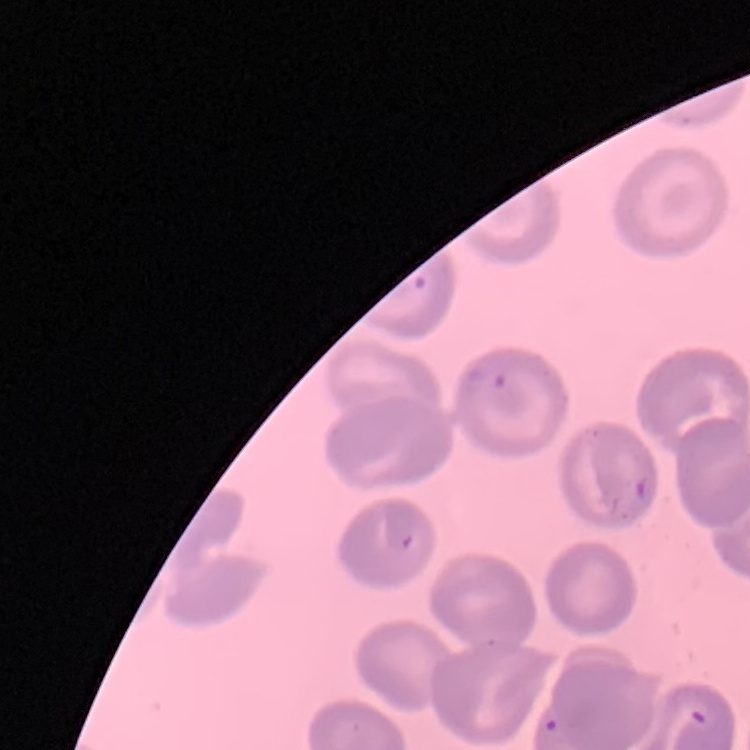

The red blood cells show no rouleaux formation. Square crop of a larger photomicrograph. Thin blood film. Stained with either Field's or Giemsa.